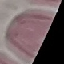

result: no malaria parasites seen
stain: Giemsa
preparation: thin blood film
image_type: cell patch, automatically extracted from a larger field of view and resized to 64 × 64 pixels
capture: smartphone camera at the microscope eyepiece